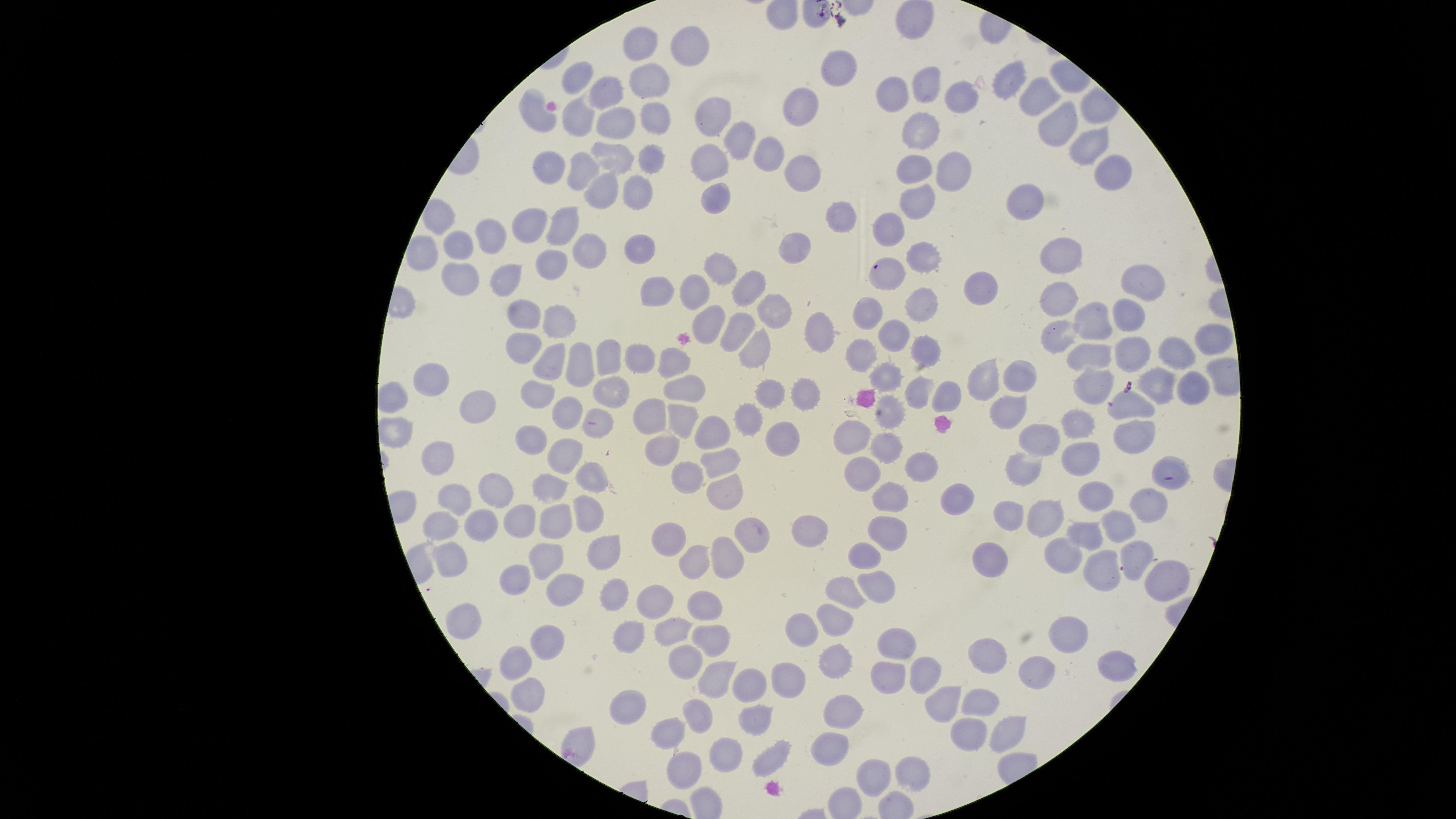
Approximate marker points, in pixels from the top-left corner. Uninfected red blood cells: (x=643, y=43), (x=689, y=51), (x=840, y=66), (x=581, y=77), (x=648, y=79), (x=929, y=82), (x=1009, y=83), (x=895, y=95), (x=609, y=97), (x=1040, y=97), (x=965, y=99), (x=803, y=102), (x=583, y=116), (x=538, y=117), (x=713, y=117), (x=655, y=119), (x=621, y=125), (x=1056, y=127), (x=919, y=129), (x=736, y=142), (x=773, y=148), (x=1079, y=150), (x=614, y=158), (x=653, y=161), (x=709, y=165), (x=920, y=168), (x=554, y=169), (x=580, y=171), (x=806, y=171), (x=959, y=171), (x=1108, y=173), (x=638, y=187), (x=605, y=189), (x=1023, y=193), (x=716, y=199), (x=919, y=203), (x=841, y=218), (x=439, y=219), (x=531, y=225), (x=563, y=225), (x=894, y=230), (x=495, y=238), (x=801, y=243), (x=461, y=247), (x=584, y=250), (x=643, y=250), (x=422, y=252), (x=1063, y=257), (x=923, y=259), (x=554, y=262), (x=724, y=269), (x=892, y=273), (x=461, y=274), (x=506, y=279), (x=1138, y=281), (x=976, y=284), (x=754, y=286), (x=697, y=289), (x=657, y=291), (x=1057, y=300), (x=921, y=307), (x=774, y=311), (x=519, y=314), (x=868, y=314), (x=1129, y=314), (x=1100, y=321), (x=563, y=323), (x=710, y=323), (x=819, y=327), (x=741, y=329), (x=895, y=330), (x=1063, y=337), (x=1212, y=342), (x=528, y=348), (x=1134, y=349), (x=762, y=353), (x=862, y=353), (x=926, y=353), (x=1095, y=354), (x=1182, y=354), (x=608, y=356), (x=553, y=362), (x=676, y=362), (x=584, y=363), (x=638, y=363), (x=1020, y=375), (x=888, y=377), (x=429, y=379), (x=985, y=381), (x=1095, y=382), (x=1163, y=382), (x=689, y=388), (x=1196, y=388), (x=612, y=390), (x=922, y=390), (x=947, y=391), (x=801, y=392), (x=539, y=394), (x=768, y=397), (x=1128, y=404), (x=483, y=406), (x=1010, y=408), (x=570, y=409), (x=651, y=415), (x=892, y=416), (x=753, y=418), (x=684, y=422), (x=1083, y=422), (x=600, y=427), (x=1134, y=429), (x=723, y=430), (x=784, y=436), (x=855, y=437), (x=534, y=438), (x=1045, y=439), (x=888, y=446), (x=665, y=447), (x=564, y=455), (x=1086, y=456), (x=437, y=459), (x=721, y=459), (x=920, y=464), (x=1021, y=467), (x=862, y=470), (x=691, y=474), (x=588, y=480), (x=555, y=489), (x=503, y=494), (x=722, y=494), (x=456, y=497), (x=1093, y=497), (x=951, y=499), (x=887, y=501), (x=1145, y=513), (x=1053, y=515), (x=1019, y=517), (x=587, y=520), (x=553, y=523), (x=1118, y=523), (x=477, y=524), (x=527, y=524), (x=445, y=527), (x=1093, y=531), (x=886, y=532), (x=669, y=533), (x=810, y=533), (x=750, y=538), (x=598, y=552), (x=992, y=554), (x=697, y=555), (x=549, y=556), (x=1058, y=556), (x=865, y=557), (x=454, y=558), (x=729, y=560), (x=1132, y=561), (x=1093, y=573), (x=1158, y=577), (x=518, y=579), (x=877, y=584), (x=564, y=587), (x=853, y=587), (x=609, y=592), (x=656, y=597), (x=704, y=603), (x=836, y=614), (x=469, y=623), (x=805, y=627), (x=1071, y=628), (x=635, y=630), (x=671, y=631), (x=710, y=638), (x=902, y=641), (x=549, y=645), (x=988, y=650), (x=520, y=658), (x=1115, y=659), (x=690, y=660), (x=836, y=660), (x=925, y=673), (x=1038, y=673), (x=887, y=675), (x=715, y=676), (x=790, y=678), (x=754, y=685), (x=531, y=692), (x=974, y=700), (x=628, y=702), (x=943, y=703), (x=847, y=705), (x=701, y=715), (x=760, y=723), (x=674, y=731), (x=996, y=731), (x=963, y=733), (x=834, y=744), (x=774, y=752), (x=726, y=755), (x=913, y=767), (x=685, y=769), (x=876, y=770). Photographed with a smartphone camera through the microscope eyepiece. The visible region is circular. Giemsa-stained preparation. Presence: no malaria parasites identified. Image is 1456×819 pixels. Thin blood smear. One field of view of the specimen.